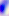
Captured at 400x magnification. Photomicrograph. Toxoplasma gondii is seen.